Point out leukocytes.
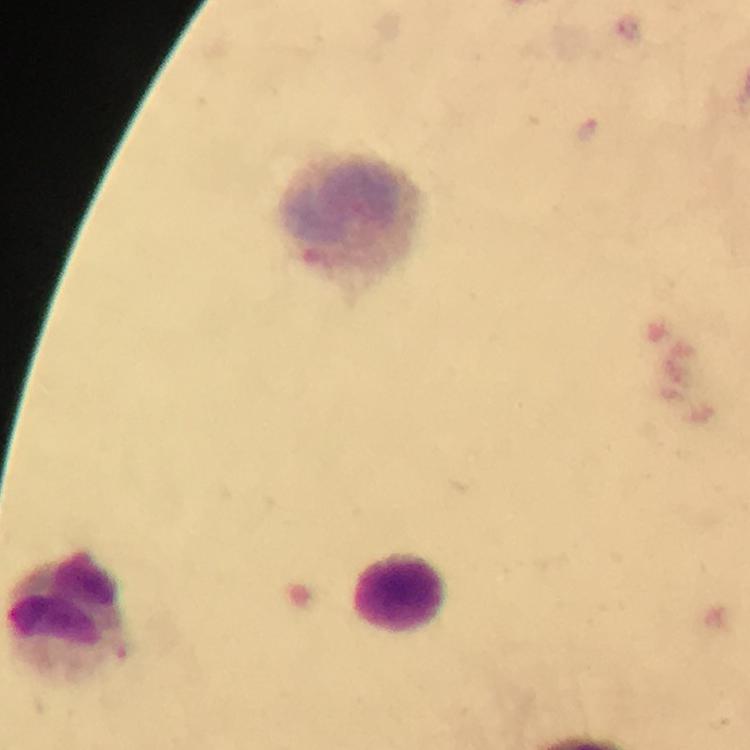

Approximate object centers, in pixels from the top-left corner.
Leukocytes: (x=348, y=218), (x=400, y=592), (x=63, y=609).

Image is 750×750 pixels. 100x magnification. From a diagnostic examination for malaria. Plasmodium parasites: none detected. A crop from one field of view. Thick smear. Giemsa-stained preparation. Photographed with a smartphone mounted on the microscope. Immersion oil applied.